Identify the cell.
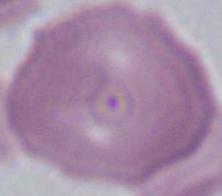

This is an erythrocyte.

Photomicrograph. 1000x magnification.